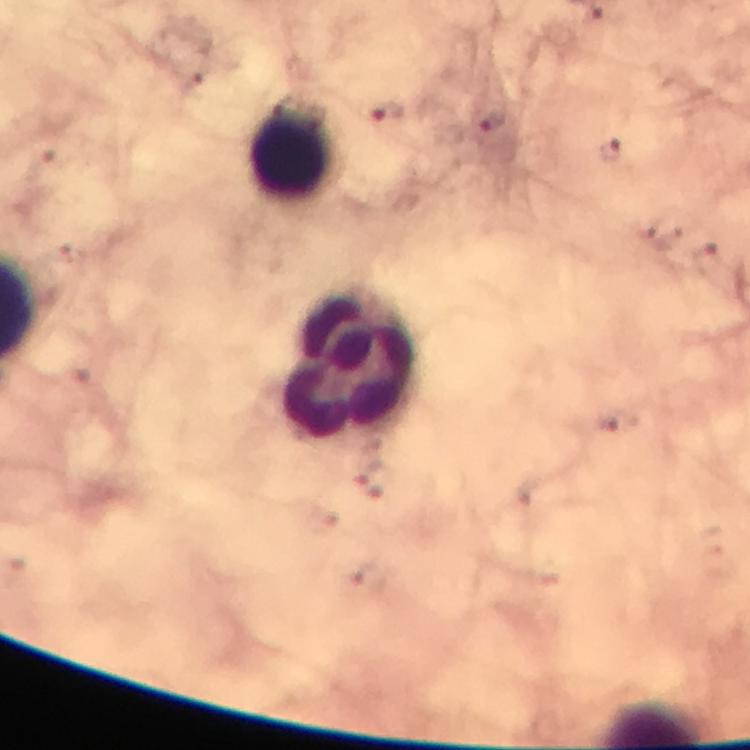

Approximate centers as {x, y} in pixels. Leukocyte locations: {292, 153}, {348, 364}. Plasmodium parasite locations: {385, 113}, {493, 123}, {609, 151}. Thick blood film. At 100x magnification. Immersion oil applied. Giemsa stain. A crop from one field of view. Photographed with a smartphone mounted on the microscope. Image is 750×750 pixels. From a malaria diagnostic workup.